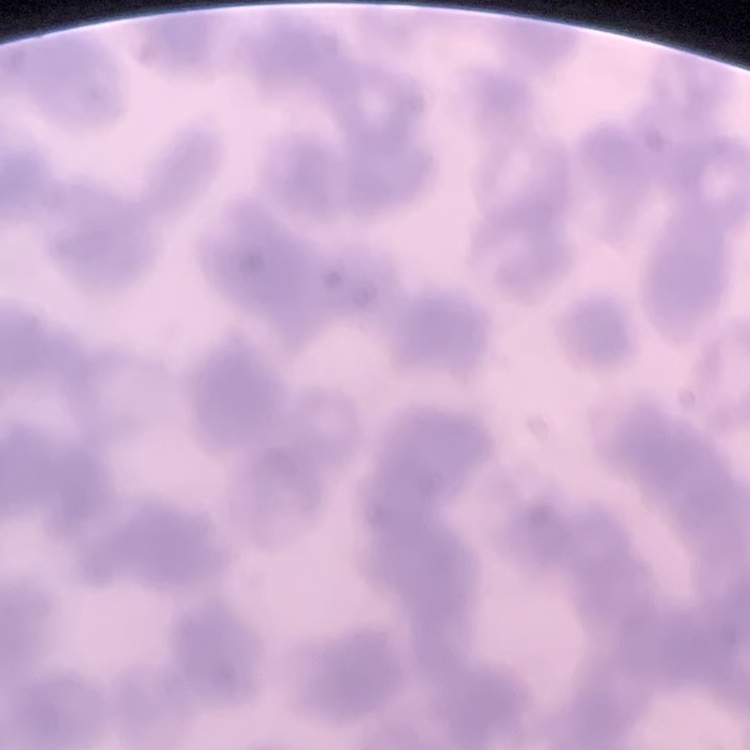

Summary:
  - Red blood cell morphology: rouleaux formation
  - Image type: square crop of a larger photomicrograph
  - Stain: Field's or Giemsa
  - Preparation: thin blood film